Assess the morphology of the red blood cells.
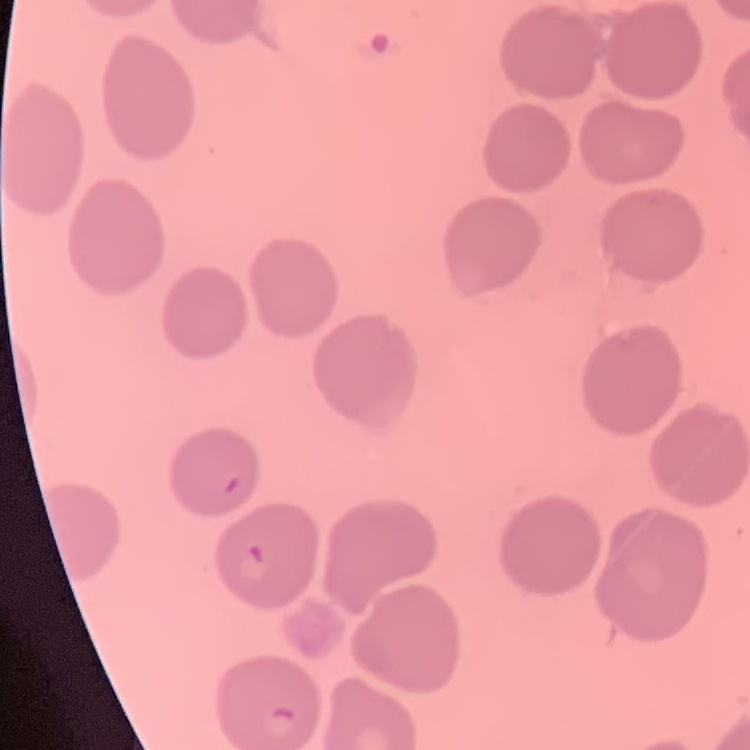

They show no rouleaux formation.

Summary:
  - Preparation: thin blood smear
  - Image type: one tile cut from a larger photomicrograph
  - Stain: Field's or Giemsa